Assess the morphology of the red blood cells.
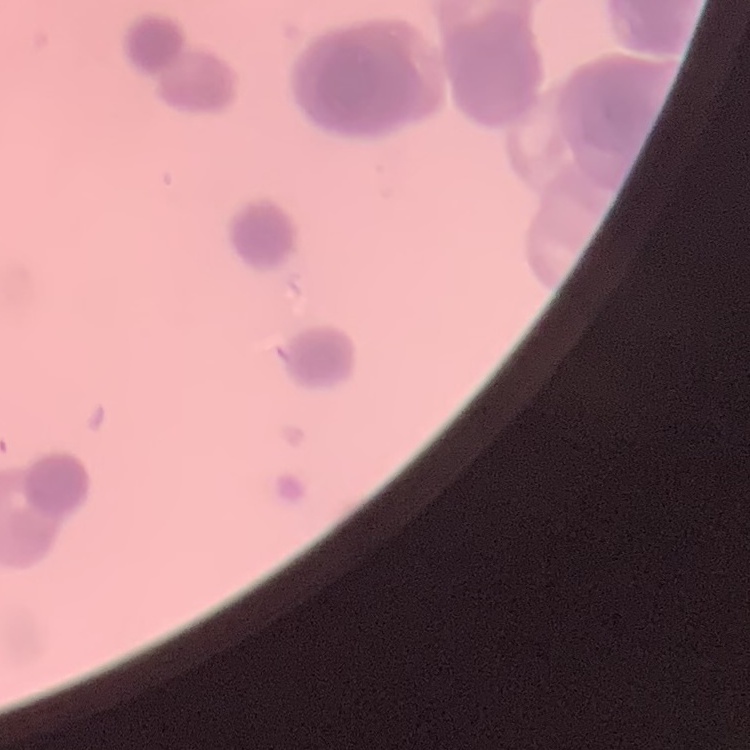
They show rouleaux formation.

Summary:
  - Preparation: thin peripheral smear
  - Stain: Field's or Giemsa
  - Image type: one tile cut from a larger photomicrograph